Point out every malaria parasite and every leukocyte.
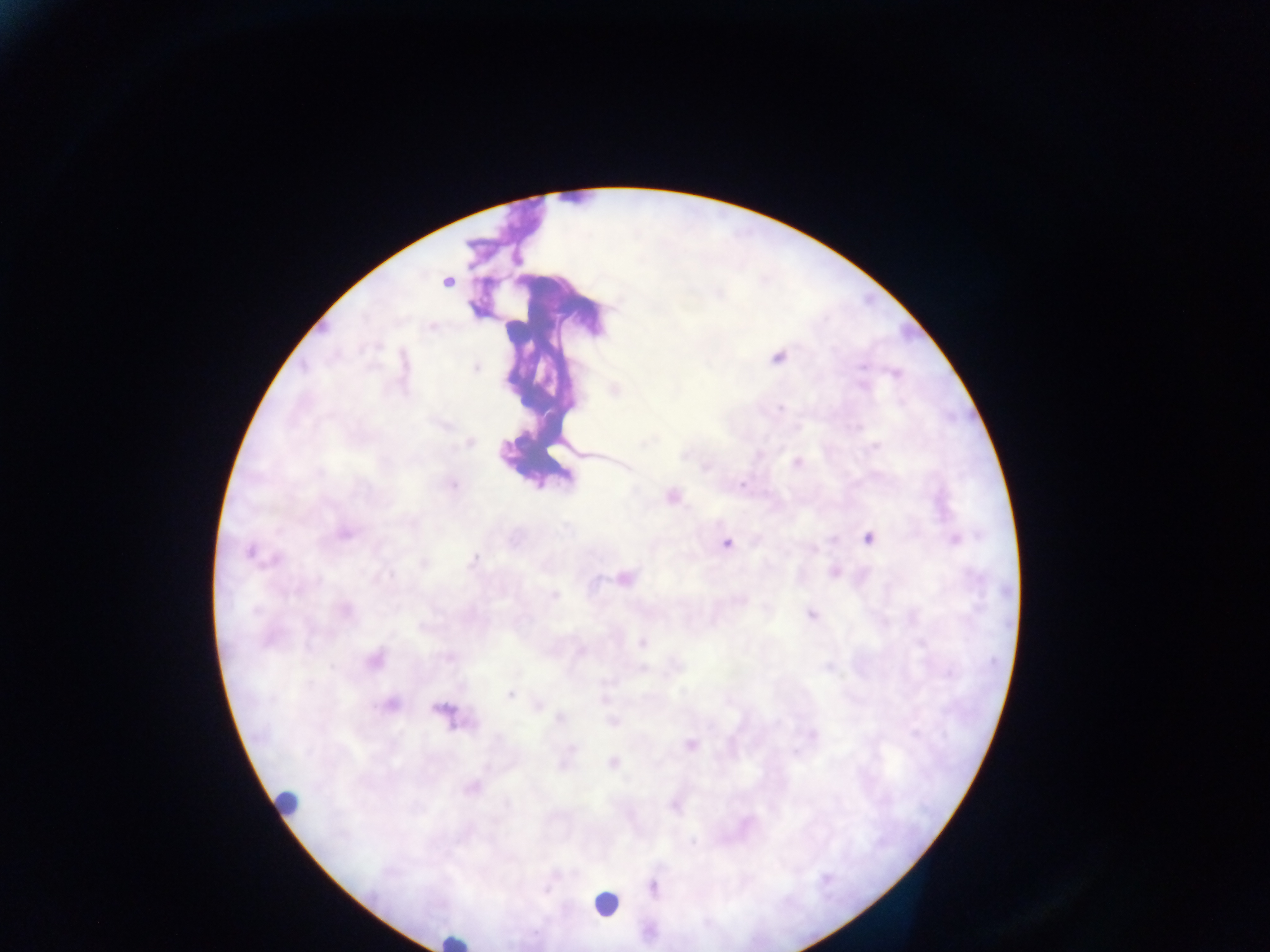

Approximate centers as (x, y) in pixels.
Malaria parasites: (639, 259), (519, 260), (447, 283), (719, 293), (431, 327), (379, 345), (779, 357), (862, 366), (477, 368), (896, 373), (862, 386), (549, 388), (572, 406), (781, 408), (857, 425), (644, 442), (470, 443), (875, 448), (553, 449), (587, 454), (685, 454), (798, 462), (706, 466), (318, 471), (453, 484), (743, 484), (672, 497), (346, 533), (867, 538), (956, 541), (726, 543), (813, 550), (250, 551), (472, 559), (274, 562), (423, 562), (835, 573), (388, 574), (595, 575), (626, 577), (555, 596), (813, 614), (641, 642), (310, 647), (447, 658), (375, 660), (330, 668), (511, 694), (538, 704), (393, 705), (377, 707), (442, 709), (559, 720), (614, 722), (915, 734), (813, 735), (691, 745), (570, 751), (614, 764), (469, 790), (508, 803), (692, 843).
Leukocytes: (280, 808), (604, 909), (454, 942).

field of view = single
preparation = thick blood smear
capture = mobile-phone photograph through a microscope
image size = 1270×952 pixels
country = Ghana